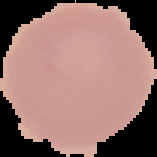

{
  "preparation": "thin blood smear",
  "image_type": "cell region segmented out of the field of view; surrounding area masked to black",
  "malaria_status": "uninfected",
  "image_size": "157×157 pixels"
}